Assess this cell for malaria.
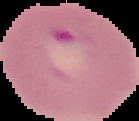

It is parasitized.

From a thin blood smear. Image is 139×121 pixels. Cell region segmented out of the field of view; the surrounding area is masked to black.